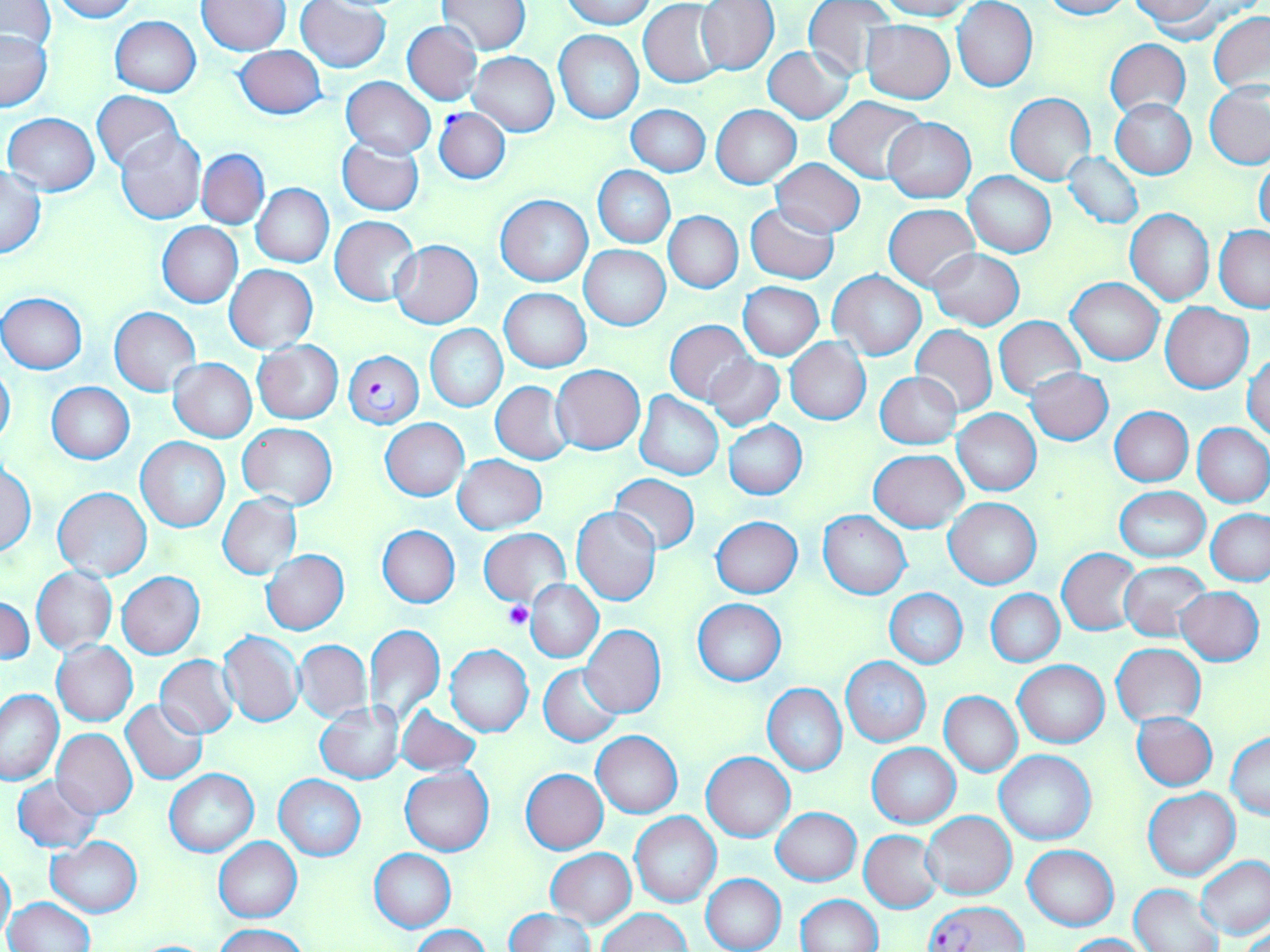

Summary:
  - Coordinate format: approximate bounding boxes as [x1, y1, x2, y2] in pixels
  - Uninfected red blood cell locations: [51, 0, 137, 22], [560, 0, 659, 28], [802, 0, 896, 80], [875, 0, 978, 20], [953, 0, 1037, 92], [1039, 0, 1131, 20], [197, 1, 289, 54], [296, 1, 390, 73], [438, 1, 532, 54], [696, 1, 779, 74], [1, 2, 57, 56], [639, 2, 725, 87], [1130, 2, 1222, 37], [1209, 11, 1270, 96], [110, 16, 200, 97], [861, 20, 955, 103], [402, 21, 481, 105], [0, 29, 52, 110], [555, 30, 644, 123], [1104, 38, 1191, 118], [234, 44, 326, 120], [763, 46, 853, 123], [469, 52, 559, 135], [342, 77, 435, 158], [1205, 82, 1270, 169], [92, 90, 183, 173], [1006, 92, 1096, 185], [825, 96, 925, 183], [1111, 97, 1197, 179], [628, 104, 710, 176], [712, 105, 801, 188], [3, 113, 100, 196], [882, 118, 976, 201], [116, 129, 206, 224], [337, 137, 424, 216], [197, 149, 269, 228], [1062, 152, 1144, 229], [771, 158, 866, 236], [1255, 158, 1270, 237], [593, 166, 675, 247], [0, 167, 46, 258], [964, 172, 1055, 257], [252, 183, 334, 268], [495, 195, 592, 286], [884, 203, 979, 290], [745, 204, 838, 284], [1125, 210, 1214, 306], [664, 212, 742, 292], [330, 215, 420, 306], [158, 222, 243, 307], [1215, 226, 1270, 312], [390, 240, 482, 328], [580, 245, 670, 329], [930, 248, 1025, 330], [224, 265, 318, 353], [829, 272, 926, 359], [1068, 277, 1163, 366], [738, 281, 824, 359], [500, 287, 591, 372], [1, 293, 87, 374], [1161, 304, 1254, 392], [110, 307, 201, 397], [993, 315, 1084, 401], [665, 320, 755, 404], [425, 324, 507, 411], [911, 325, 997, 416], [786, 338, 871, 424], [254, 340, 343, 423], [1244, 352, 1270, 439], [707, 356, 784, 431], [168, 359, 257, 442], [0, 365, 15, 448], [551, 365, 645, 454], [1026, 368, 1114, 445], [876, 372, 961, 448], [491, 381, 574, 465], [47, 382, 135, 464], [635, 392, 723, 480], [1110, 407, 1193, 486], [952, 409, 1041, 496], [380, 418, 469, 500], [724, 420, 807, 499], [1193, 422, 1270, 507], [237, 423, 337, 510], [137, 437, 229, 532], [870, 449, 968, 532], [453, 455, 547, 534], [1, 462, 36, 557], [610, 473, 698, 553], [53, 487, 151, 580], [1115, 487, 1209, 562], [218, 495, 301, 578], [944, 498, 1041, 590], [572, 507, 662, 605], [1206, 509, 1270, 585], [818, 511, 910, 599], [711, 517, 803, 598], [378, 526, 459, 607], [478, 529, 570, 607], [1058, 548, 1141, 634], [262, 551, 348, 633], [1119, 562, 1211, 640], [31, 566, 117, 654], [117, 572, 204, 659], [526, 580, 602, 662], [1175, 588, 1264, 665], [885, 589, 967, 668], [987, 590, 1064, 666], [1, 597, 34, 666], [693, 598, 787, 686], [364, 624, 445, 724], [581, 626, 665, 717], [217, 631, 304, 727], [295, 640, 372, 722], [52, 641, 138, 726], [1112, 643, 1206, 727], [445, 646, 533, 737], [155, 656, 238, 737], [840, 657, 931, 747], [1013, 660, 1109, 748], [539, 664, 624, 746], [763, 684, 847, 776], [1, 687, 65, 785], [939, 691, 1021, 777], [122, 700, 207, 783], [315, 702, 406, 783], [395, 705, 481, 774], [1132, 712, 1218, 790], [52, 729, 138, 819], [592, 731, 682, 817], [1226, 732, 1270, 819], [867, 743, 960, 828], [994, 748, 1096, 845], [702, 752, 795, 841], [400, 767, 493, 856], [521, 768, 607, 853], [165, 769, 258, 857], [12, 775, 103, 852], [275, 775, 365, 860], [1144, 788, 1240, 881], [772, 807, 860, 886], [921, 812, 1016, 899], [630, 813, 721, 908], [860, 831, 942, 913], [46, 837, 142, 916], [215, 838, 302, 921], [1022, 844, 1118, 930], [369, 848, 456, 932], [547, 849, 636, 927], [1196, 855, 1270, 939], [0, 858, 15, 945], [701, 874, 785, 952], [1131, 883, 1225, 952], [795, 894, 882, 952], [3, 898, 96, 952], [505, 908, 594, 952], [598, 909, 689, 951], [214, 923, 305, 952], [410, 925, 490, 952], [1063, 933, 1151, 951]
  - Plasmodium falciparum-infected red blood cell locations: [435, 107, 512, 184], [343, 350, 424, 430], [925, 900, 1028, 951]
  - Platelet locations: [505, 600, 534, 629]
  - Slide-level diagnosis: Plasmodium falciparum
  - Magnification: 1000x
  - Stain: May-Grünwald-Giemsa
  - Field of view: single
  - Image size: 1270×952 pixels
  - Modality: optical microscopy
  - Preparation: thin blood smear